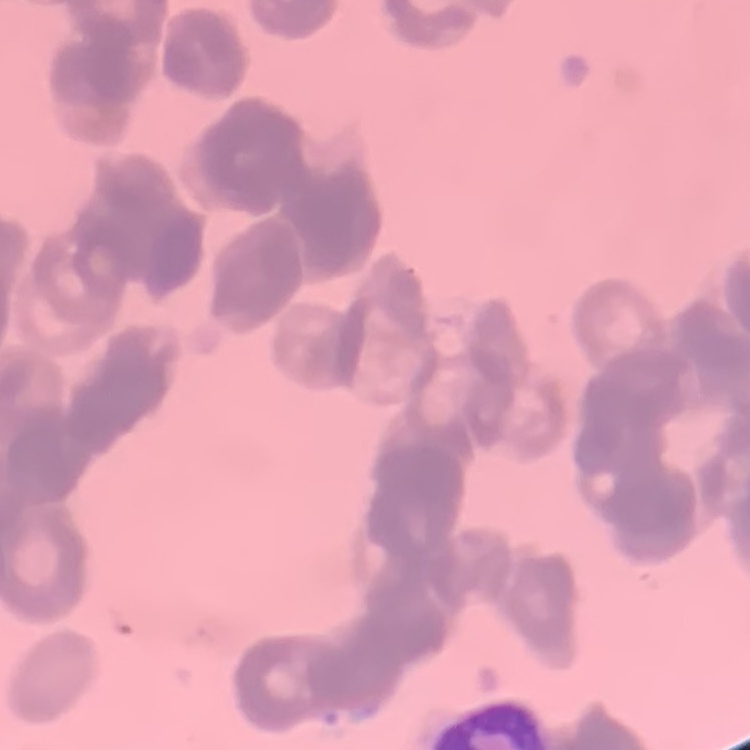
The red blood cells show rouleaux formation. One tile cut from a larger photomicrograph. Stained with either Field's or Giemsa. Thin blood smear.